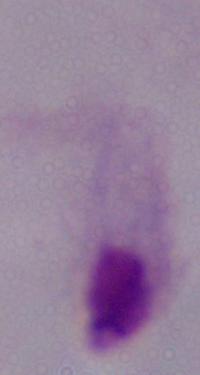

Summary:
  - Magnification: 1000x
  - Modality: micrograph
  - Identification: trichomonad